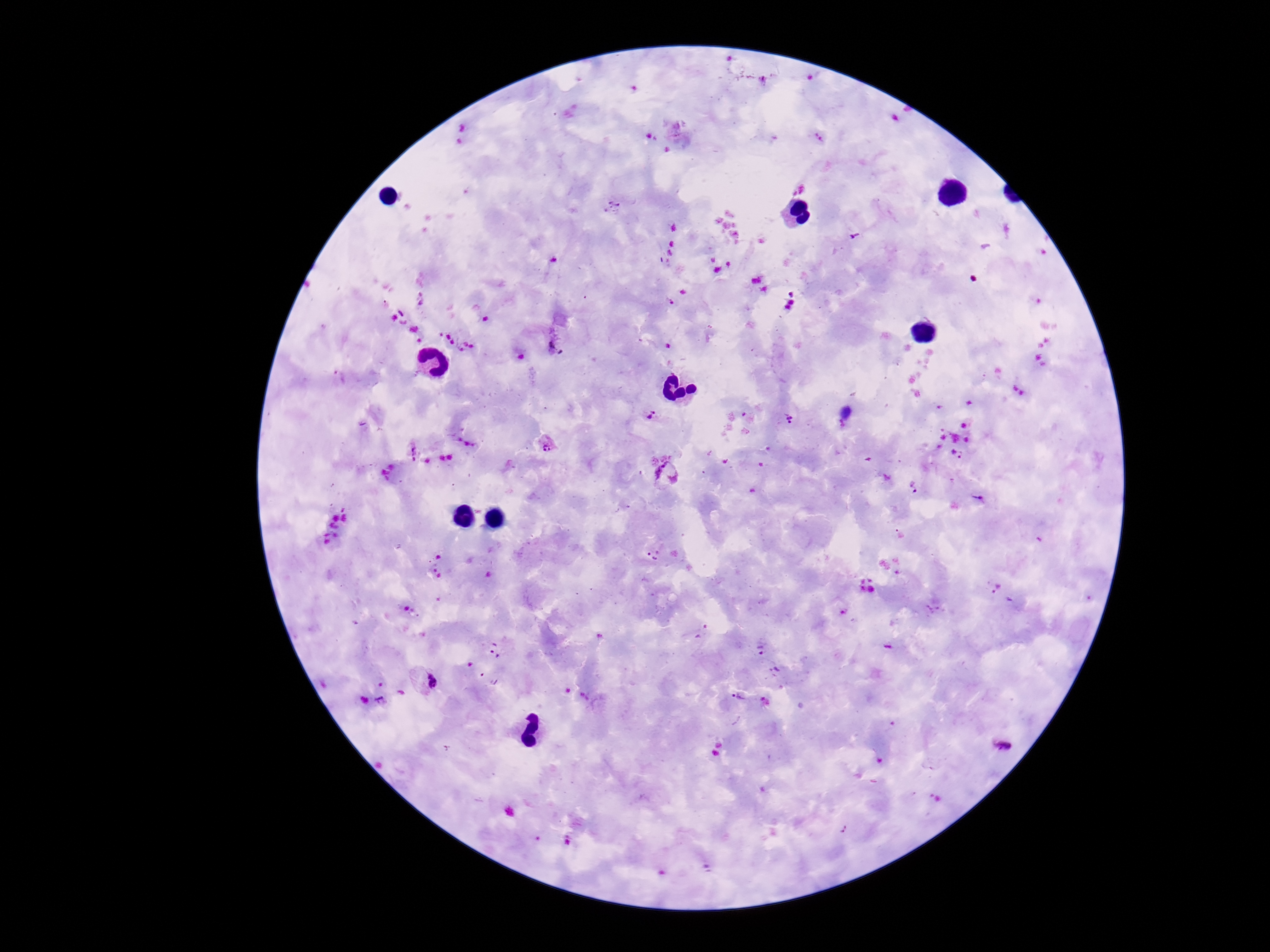 Approximate centers as [x, y] in pixels. Plasmodium parasite locations: [820, 138], [555, 349], [651, 416], [788, 420], [547, 444], [413, 453], [956, 455], [668, 475], [915, 487], [979, 498], [762, 649], [496, 650], [423, 683], [739, 697], [1002, 745], [843, 828]. Smartphone photograph taken through the microscope eyepiece. One field from this slide. Thick peripheral-blood smear. Image is 1270×952 pixels. Giemsa stain. 100x magnification. Patient malaria status: infected.